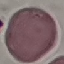

result = negative for malaria parasites
preparation = thin blood film
image type = cell patch, automatically extracted from a larger field of view and resized to 64 × 64 pixels
stain = Giemsa
capture = smartphone through the microscope eyepiece